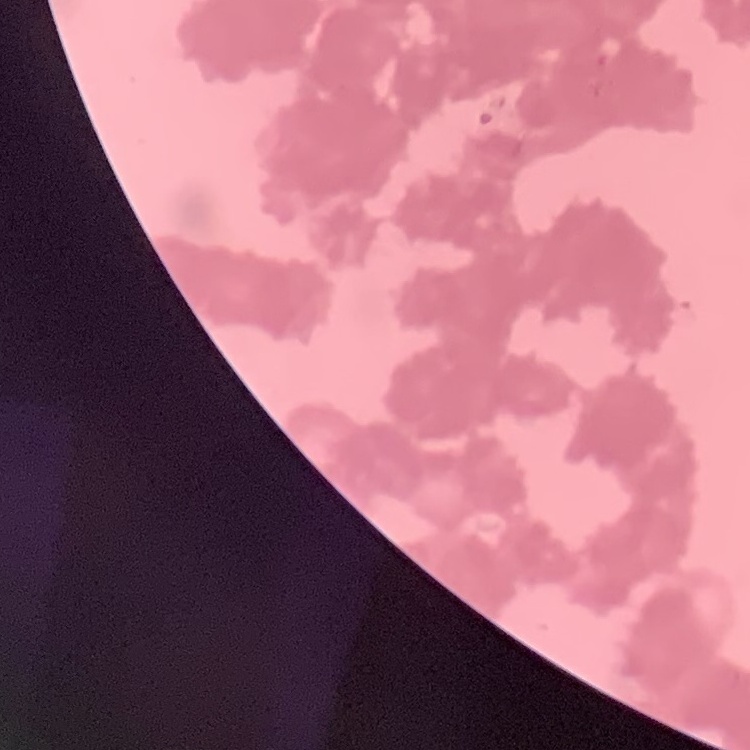
The erythrocytes show rouleaux formation. Stained with either Field's or Giemsa. Thin blood film. One tile cut from a larger photomicrograph.